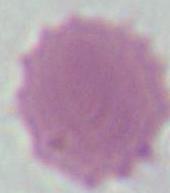

magnification: 1000x
identification: red blood cell
modality: photomicrograph